Look for Plasmodium parasites.
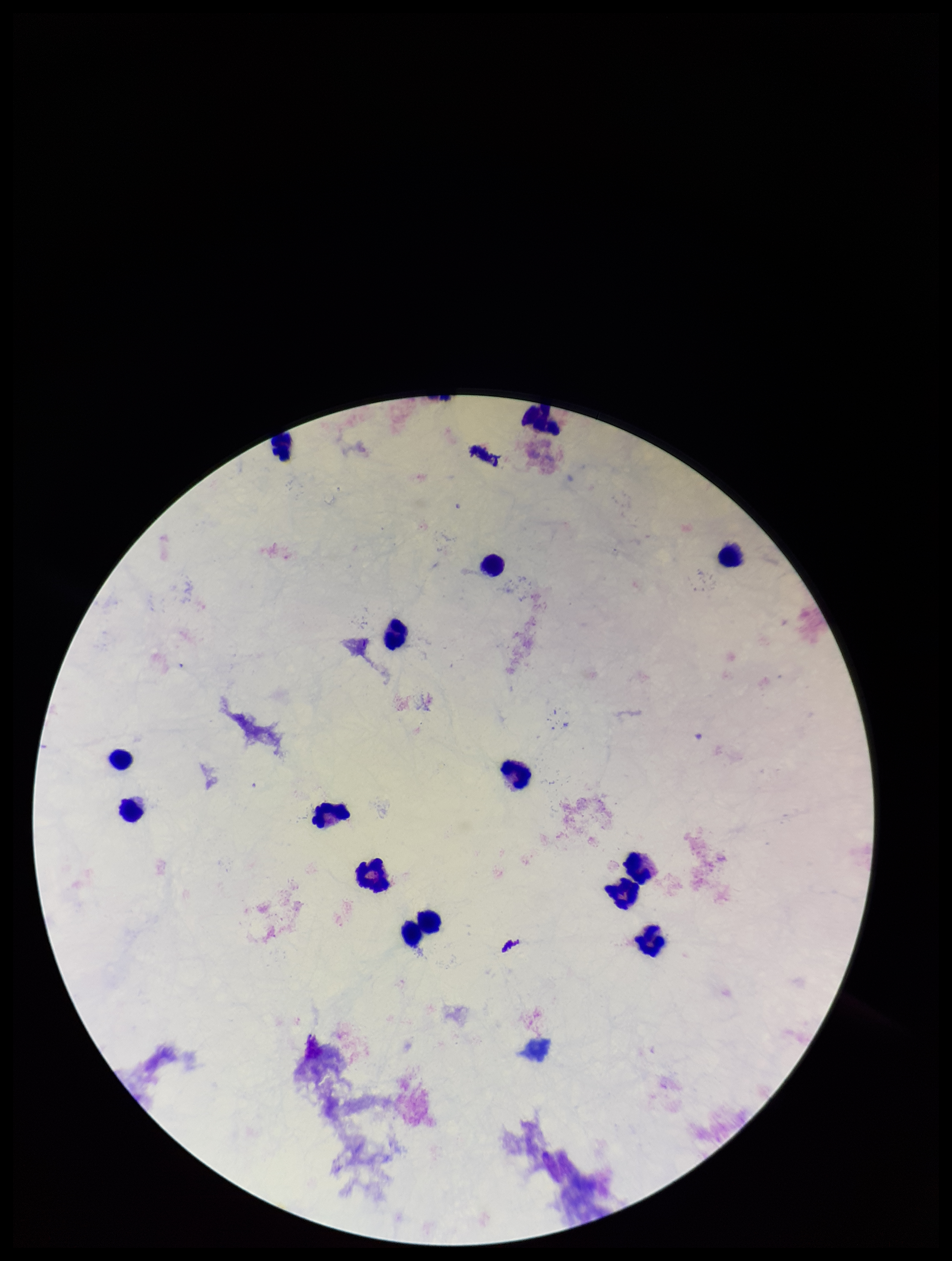
None identified.

Image is 952×1261 pixels. Stained with Giemsa. Patient malaria status: negative. Leukocyte count: 15. Photographed through the microscope eyepiece with a smartphone camera. Parasite count: 0. Preparation: thick blood smear. One field from this slide.